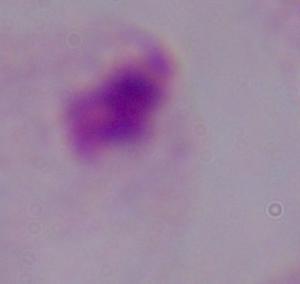 Photomicrograph. A trichomonad is shown. Captured at 1000x magnification.